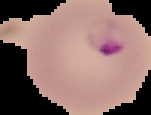
Summary:
  - Image type: cell region segmented out of the field of view; surrounding area masked to black
  - Image size: 151×115 pixels
  - Preparation: thin blood film
  - Malaria status: parasitized